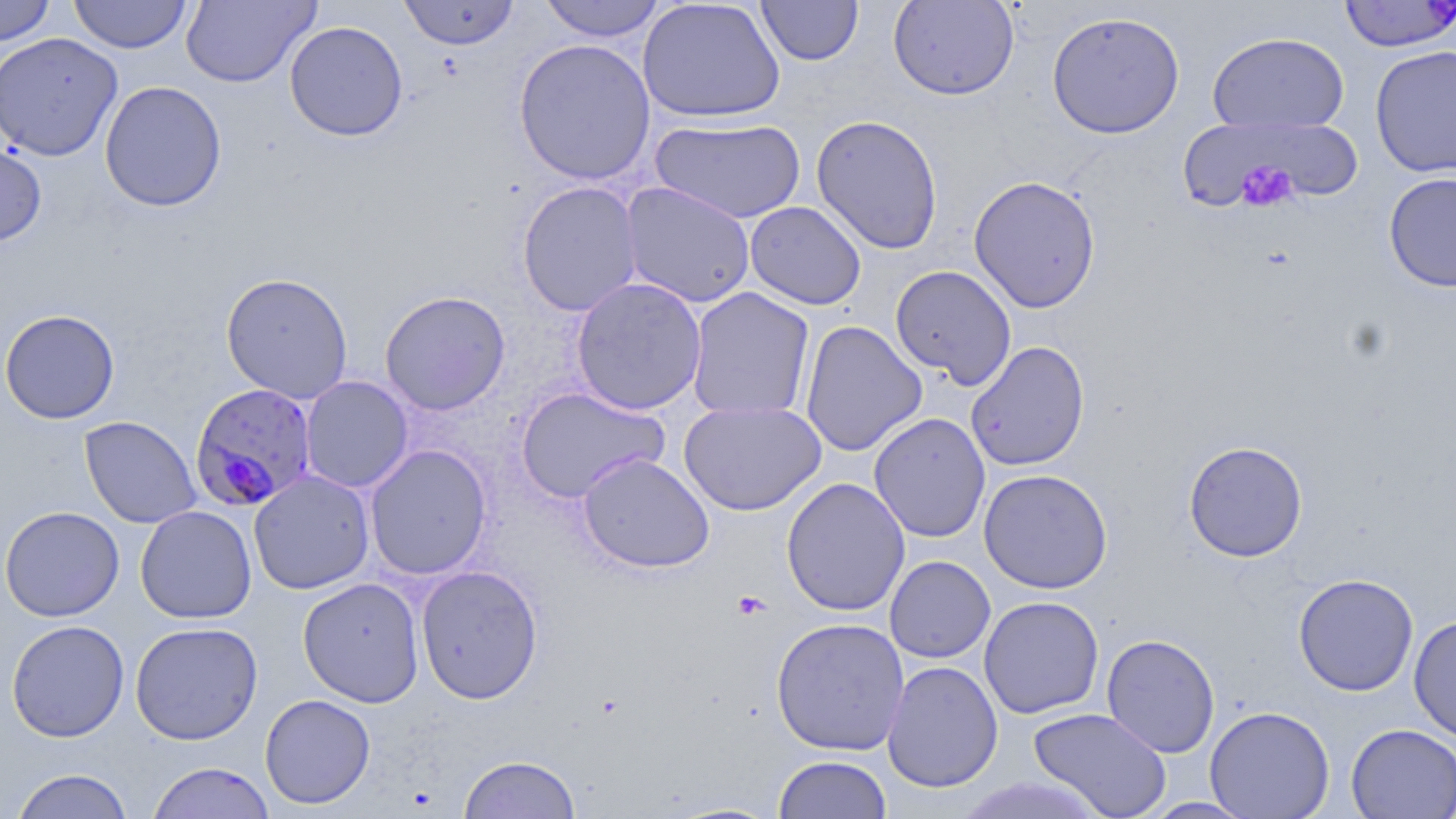

Summary:
  - Coordinate format: approximate bounding boxes as [x1, y1, x2, y2] in pixels
  - Uninfected red blood cell locations: [0, 0, 56, 46], [66, 0, 318, 58], [69, 0, 192, 54], [180, 0, 320, 88], [398, 0, 521, 50], [538, 0, 667, 42], [756, 0, 863, 66], [888, 0, 1019, 100], [638, 1, 786, 123], [1047, 10, 1185, 139], [284, 21, 409, 142], [1207, 31, 1349, 134], [0, 32, 123, 161], [513, 38, 656, 185], [1369, 45, 1456, 179], [99, 80, 227, 212], [810, 114, 944, 254], [650, 117, 806, 224], [1192, 118, 1350, 213], [0, 137, 47, 247], [1384, 172, 1456, 292], [968, 175, 1101, 313], [517, 181, 643, 317], [620, 182, 756, 308], [744, 201, 866, 310], [890, 265, 1017, 389], [221, 272, 353, 403], [570, 277, 708, 416], [686, 286, 815, 422], [380, 290, 511, 415], [0, 309, 120, 424], [799, 320, 926, 456], [965, 340, 1090, 471], [300, 376, 413, 493], [516, 386, 669, 503], [679, 400, 826, 515], [869, 413, 991, 542], [80, 416, 201, 528], [1183, 441, 1308, 562], [365, 444, 491, 579], [578, 451, 715, 573], [978, 468, 1113, 594], [248, 469, 374, 595], [781, 477, 911, 616], [0, 505, 125, 622], [135, 505, 257, 624], [885, 556, 995, 663], [415, 564, 543, 704], [1293, 573, 1419, 696], [298, 577, 424, 707], [979, 595, 1104, 719], [1408, 614, 1456, 743], [770, 616, 910, 756], [5, 620, 130, 742], [130, 621, 263, 744], [1101, 633, 1220, 758], [882, 661, 1003, 792], [260, 693, 376, 809], [1205, 705, 1335, 818], [1028, 707, 1172, 819], [1346, 723, 1456, 818], [458, 754, 581, 818], [773, 755, 892, 819], [146, 761, 276, 819], [10, 768, 135, 818], [954, 777, 1111, 818], [1139, 797, 1260, 818]
  - Platelet locations: [1235, 161, 1298, 213], [732, 590, 771, 620]
  - Plasmodium falciparum-infected red blood cell locations: [1338, 1, 1455, 51], [190, 382, 319, 512]
  - Slide-level diagnosis: Plasmodium falciparum
  - Magnification: 1000x
  - Image size: 1456×819 pixels
  - Field of view: one of a larger specimen
  - Modality: optical microscopy
  - Stain: May-Grünwald-Giemsa
  - Preparation: thin blood smear